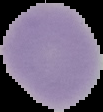
{
  "result": "negative for Plasmodium parasites",
  "image_size": "103×112 pixels",
  "preparation": "thin blood smear",
  "image_type": "cell region segmented out of the field of view; surrounding area masked to black"
}